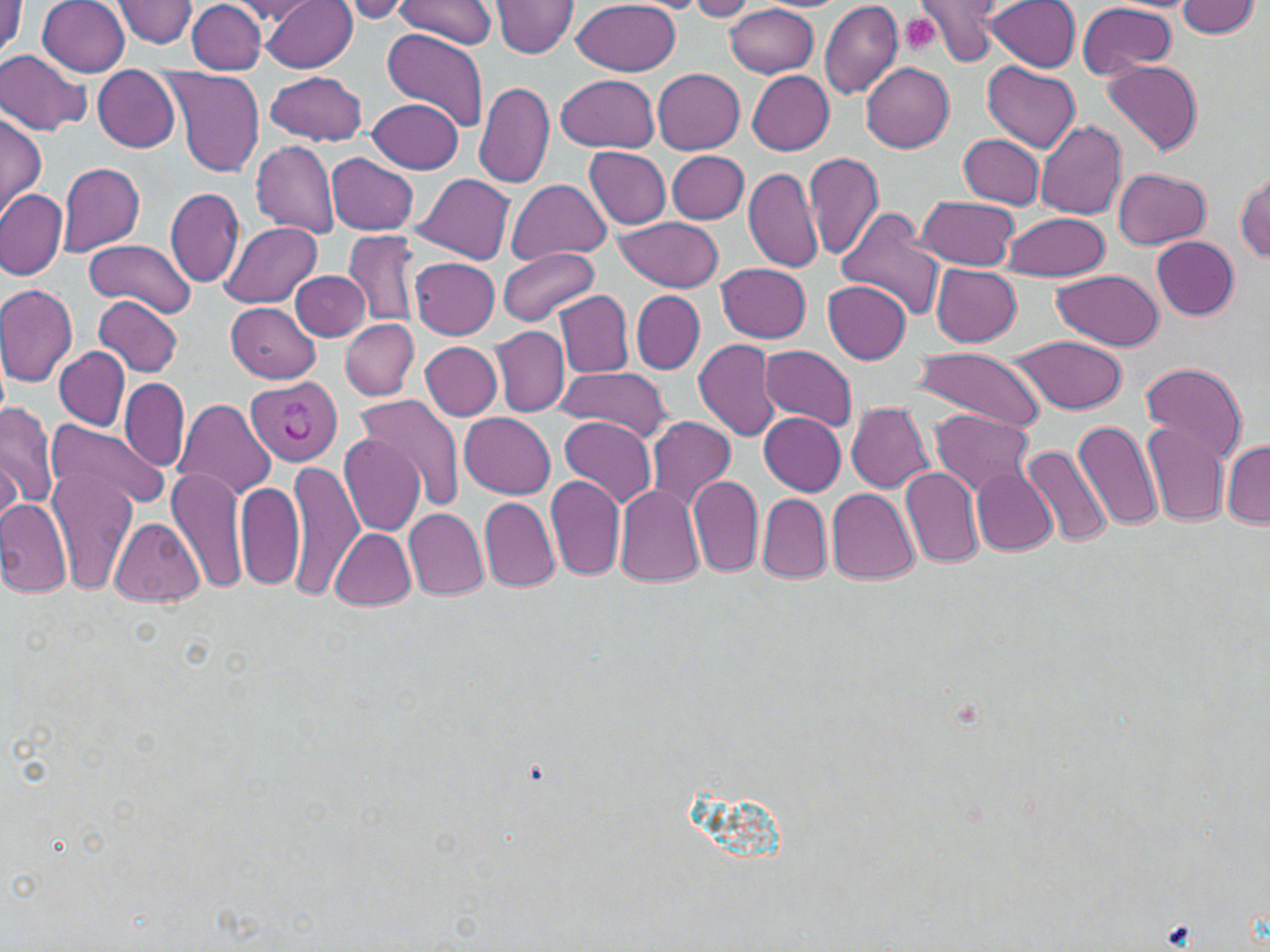 Approximate bounding boxes as (x1, y1, x2, y2) in pixels. Uninfected red blood cell locations: (0, 0, 22, 64), (38, 0, 131, 75), (112, 0, 199, 47), (262, 0, 359, 73), (337, 0, 412, 22), (398, 0, 499, 50), (573, 0, 680, 76), (684, 0, 759, 21), (818, 0, 905, 101), (919, 0, 1010, 65), (983, 0, 1082, 71), (187, 1, 265, 72), (229, 1, 322, 23), (1175, 1, 1260, 38), (491, 2, 578, 58), (725, 4, 819, 78), (1075, 4, 1177, 80), (383, 30, 488, 134), (0, 51, 91, 135), (1102, 59, 1203, 156), (861, 61, 954, 152), (983, 61, 1080, 152), (92, 67, 180, 153), (161, 67, 265, 178), (654, 68, 745, 154), (266, 70, 367, 145), (747, 71, 835, 155), (557, 74, 661, 153), (473, 80, 555, 190), (369, 98, 464, 173), (0, 112, 46, 218), (1035, 121, 1128, 219), (958, 134, 1045, 209), (249, 139, 341, 239), (584, 146, 671, 228), (666, 150, 749, 223), (805, 151, 884, 261), (327, 153, 419, 235), (57, 162, 146, 256), (744, 167, 825, 273), (1114, 167, 1210, 250), (1235, 169, 1270, 262), (413, 173, 515, 264), (507, 179, 612, 264), (165, 187, 244, 289), (0, 188, 68, 281), (916, 195, 1020, 269), (835, 210, 946, 320), (1001, 211, 1110, 282), (614, 216, 725, 292), (221, 221, 324, 307), (344, 228, 420, 328), (1151, 236, 1240, 320), (85, 238, 196, 318), (497, 248, 600, 325), (411, 257, 499, 339), (716, 262, 812, 344), (932, 264, 1022, 347), (1051, 267, 1164, 352), (292, 270, 371, 341), (822, 282, 911, 363), (0, 285, 77, 388), (554, 291, 634, 378), (631, 291, 705, 373), (93, 296, 184, 376), (228, 302, 321, 383), (339, 319, 419, 399), (489, 326, 570, 418), (1008, 334, 1127, 415), (693, 338, 780, 442), (421, 341, 502, 419), (759, 345, 858, 429), (911, 345, 1047, 433), (56, 346, 130, 430), (1140, 361, 1249, 465), (556, 365, 671, 441), (120, 378, 188, 471), (355, 395, 463, 513), (171, 398, 277, 501), (1, 401, 57, 515), (845, 401, 934, 492), (931, 410, 1034, 498), (460, 412, 556, 497), (760, 412, 846, 496), (560, 415, 656, 509), (644, 415, 737, 514), (47, 418, 166, 511), (1074, 419, 1165, 537), (1142, 424, 1229, 529), (340, 432, 426, 536), (1222, 439, 1270, 529), (1021, 442, 1113, 549), (1, 450, 22, 527), (288, 459, 364, 600), (46, 465, 137, 597), (901, 465, 985, 570), (167, 466, 248, 598), (972, 468, 1058, 555), (545, 475, 626, 583), (687, 475, 763, 579), (236, 479, 305, 591), (614, 483, 707, 587), (826, 487, 920, 585), (758, 493, 832, 584), (480, 495, 561, 593), (0, 496, 72, 600), (403, 507, 489, 602), (108, 518, 205, 607), (328, 526, 417, 609). Plasmodium vivax-infected red blood cell locations: (246, 377, 344, 465). Platelet locations: (901, 15, 943, 55), (1162, 919, 1194, 948). Slide-level diagnosis: Plasmodium vivax. Light microscopy. Thin blood film. One field of a larger specimen. May-Grünwald-Giemsa stain. 1000x magnification. Image is 1270×952 pixels.